Classify this cell by malaria status.
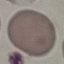
Uninfected.

{
  "preparation": "thin smear",
  "stain": "Giemsa",
  "image_type": "automatically extracted cell patch, resized to 64 × 64 pixels",
  "capture": "smartphone camera at the microscope eyepiece"
}